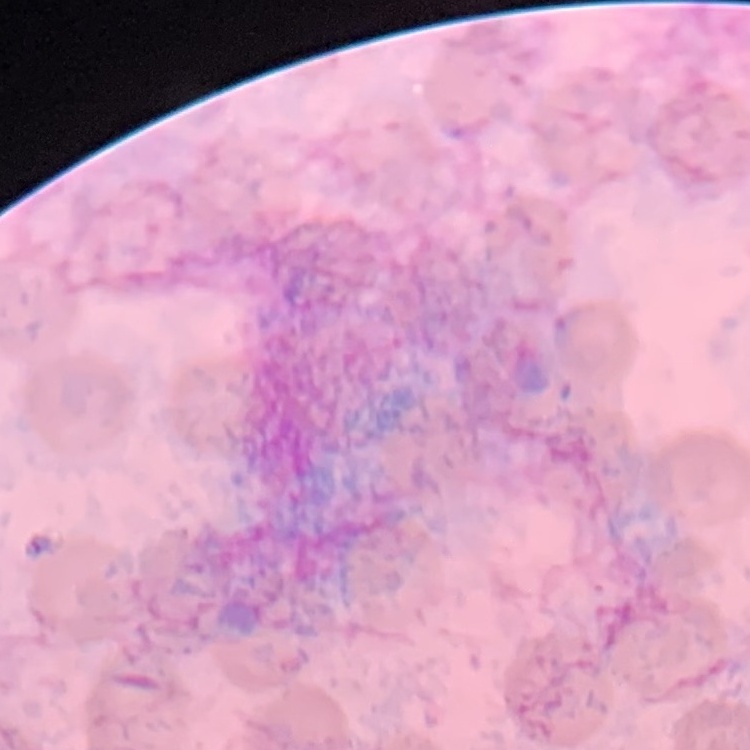
{
  "erythrocyte_morphology": "no rouleaux formation",
  "stain": "Field's or Giemsa",
  "image_type": "square crop of a larger photomicrograph",
  "preparation": "thin peripheral smear"
}